Describe the morphology of the erythrocytes.
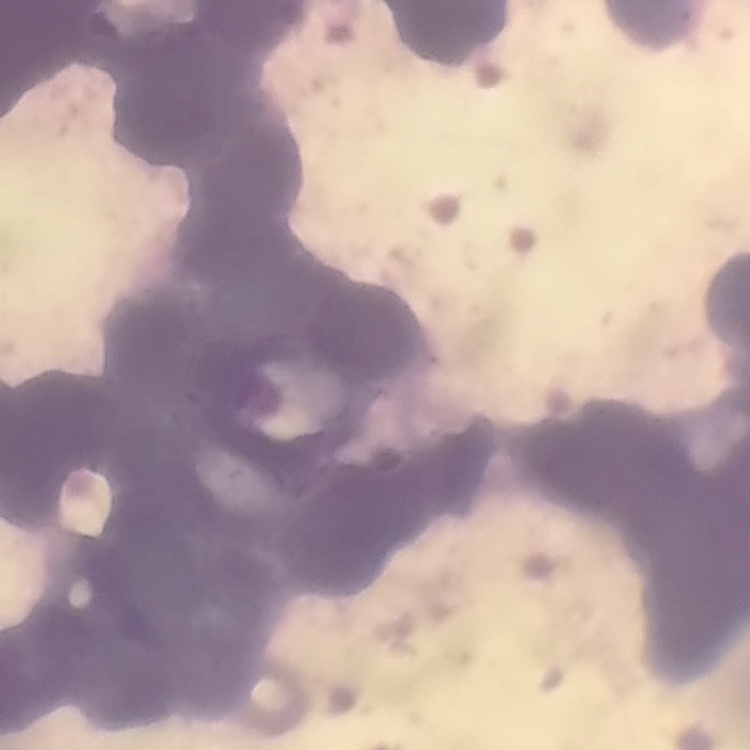

Rouleaux formation.

Thin blood film. Field's or Giemsa stain. One tile cut from a larger photomicrograph.